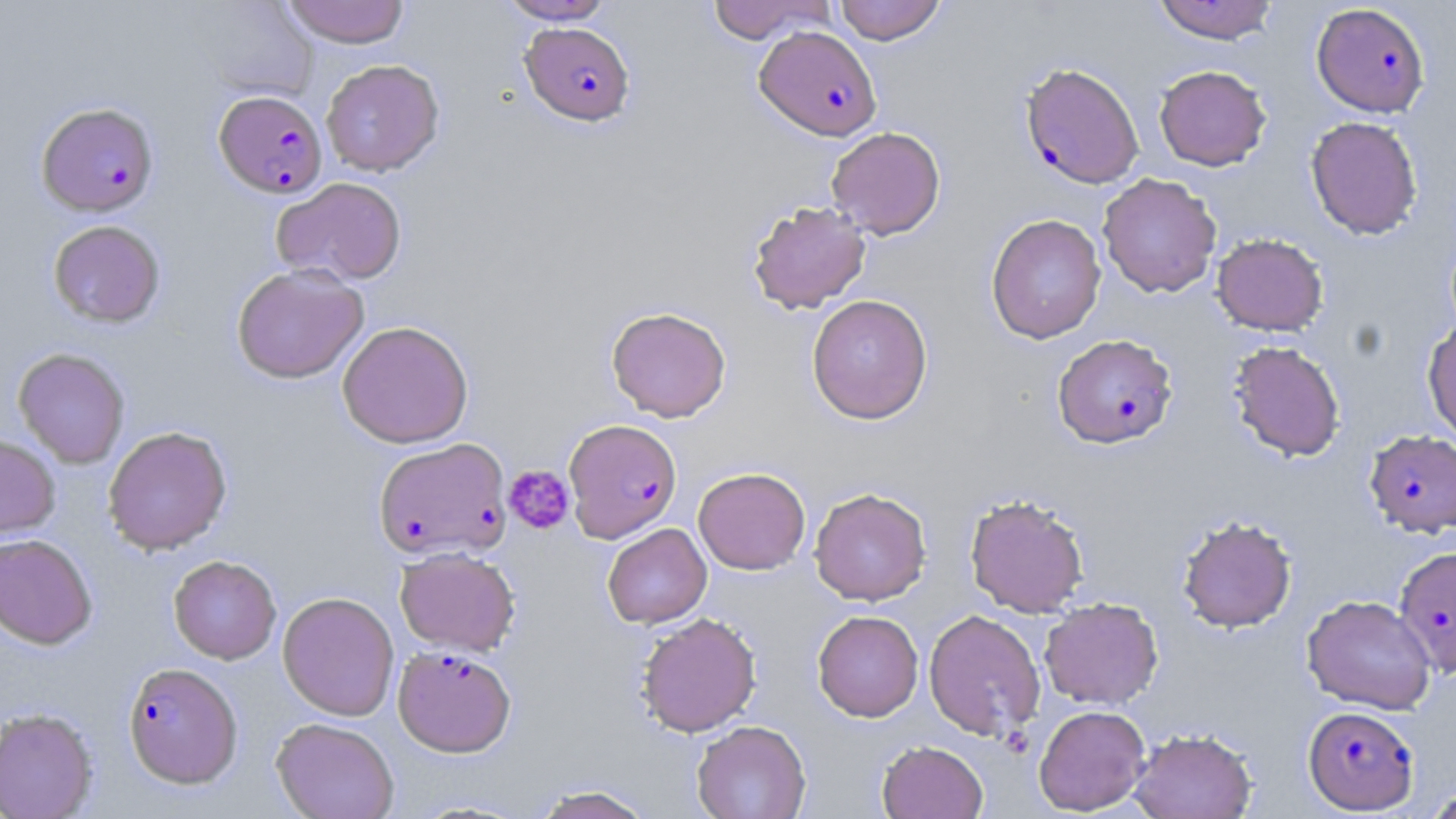 Approximate bounding boxes as [x1, y1, x2, y2] in pixels. Plasmodium falciparum-infected red blood cell locations: [1312, 3, 1431, 117], [521, 23, 635, 126], [753, 26, 882, 141], [1019, 61, 1144, 188], [213, 89, 327, 198], [36, 101, 159, 216], [1053, 334, 1178, 449], [564, 418, 682, 542], [1364, 429, 1456, 537], [373, 437, 512, 561], [1393, 544, 1456, 677], [393, 645, 516, 757], [123, 662, 243, 788], [1303, 705, 1419, 814]. Platelet locations: [503, 464, 575, 534]. Uninfected red blood cell locations: [282, 0, 410, 47], [497, 0, 616, 24], [707, 0, 834, 44], [834, 0, 946, 45], [1152, 1, 1279, 44], [191, 3, 321, 100], [321, 59, 444, 176], [1153, 65, 1271, 171], [1305, 115, 1423, 240], [826, 127, 946, 239], [1097, 172, 1222, 298], [271, 177, 407, 286], [747, 201, 871, 314], [986, 213, 1107, 344], [47, 220, 165, 328], [1212, 233, 1329, 336], [231, 264, 369, 384], [807, 294, 933, 424], [606, 306, 731, 422], [1422, 318, 1456, 444], [337, 320, 473, 448], [1227, 340, 1346, 462], [13, 347, 130, 468], [103, 425, 232, 555], [0, 434, 61, 539], [693, 467, 810, 575], [809, 487, 932, 606], [964, 492, 1090, 617], [1176, 515, 1297, 633], [602, 523, 712, 629], [0, 534, 97, 649], [395, 547, 520, 655], [168, 555, 281, 664], [277, 591, 399, 721], [1302, 594, 1437, 714], [1039, 597, 1163, 710], [924, 609, 1045, 741], [812, 610, 923, 722], [635, 612, 762, 737], [1033, 704, 1151, 815], [0, 707, 98, 819], [271, 717, 399, 819], [691, 720, 811, 819], [1129, 728, 1257, 819], [876, 740, 988, 819], [529, 784, 657, 819], [1422, 786, 1456, 818]. Slide-level diagnosis: Plasmodium falciparum. Light microscopy. 1000x magnification. Image is 1456×819 pixels. May-Grünwald-Giemsa stain. Thin blood film. One field of a larger specimen.